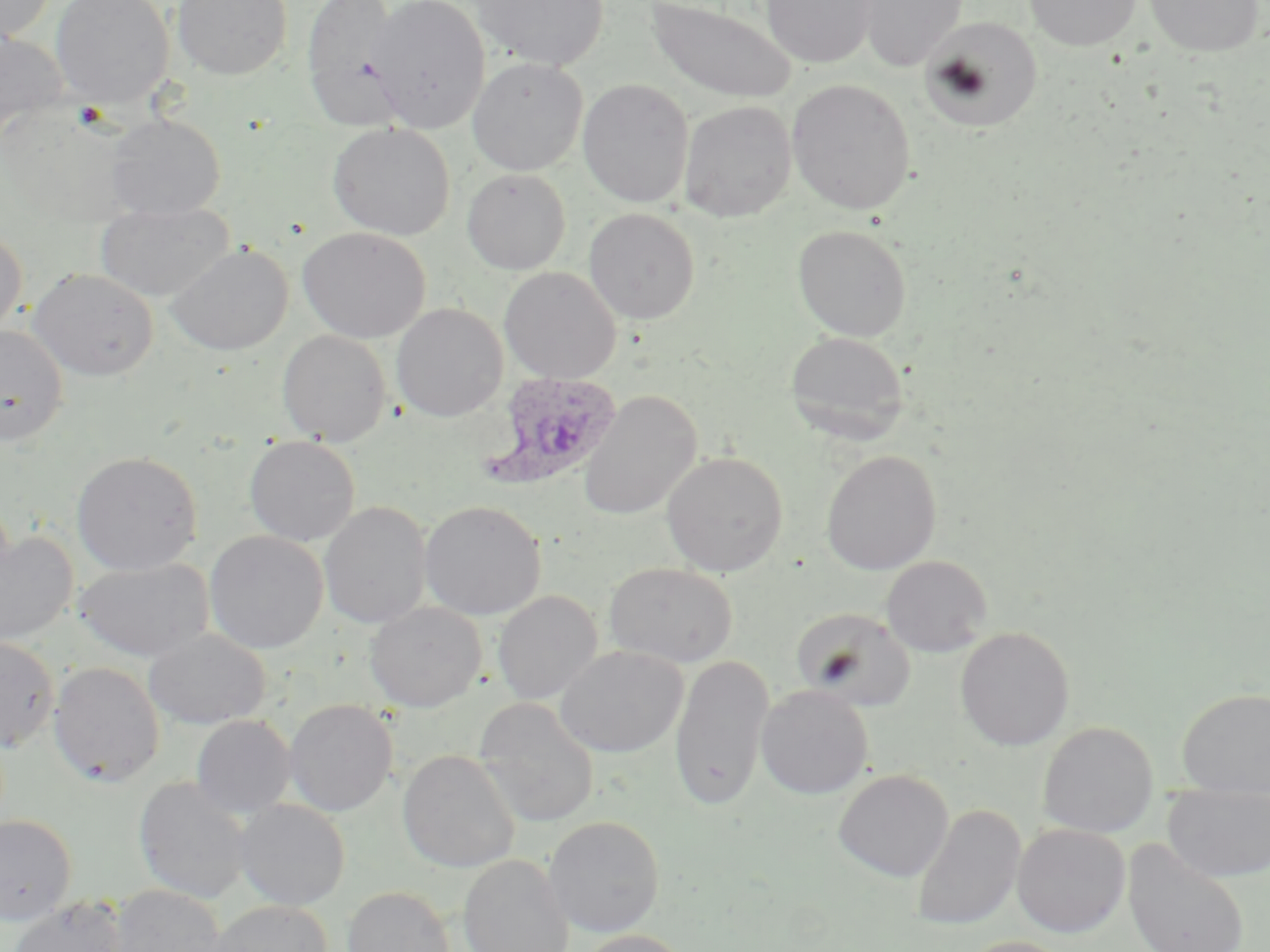

Summary:
  - Coordinate format: approximate bounding boxes as [x1, y1, x2, y2] in pixels
  - Plasmodium ovale-infected red blood cell locations: [478, 371, 623, 491]
  - Uninfected red blood cell locations: [0, 0, 55, 42], [50, 0, 175, 108], [172, 0, 292, 80], [300, 0, 409, 131], [367, 0, 490, 133], [470, 0, 609, 71], [761, 0, 876, 68], [857, 0, 965, 72], [1023, 0, 1141, 51], [1143, 0, 1264, 57], [645, 1, 797, 104], [921, 17, 1043, 132], [0, 30, 69, 145], [467, 57, 587, 175], [577, 78, 694, 208], [787, 79, 917, 215], [679, 100, 797, 223], [106, 114, 226, 221], [327, 122, 455, 240], [462, 168, 571, 274], [95, 200, 235, 302], [583, 208, 700, 324], [792, 224, 911, 341], [0, 227, 27, 337], [297, 227, 431, 342], [166, 244, 293, 355], [499, 266, 622, 384], [28, 267, 159, 381], [391, 302, 508, 421], [0, 324, 68, 446], [277, 329, 392, 446], [785, 330, 909, 443], [578, 390, 702, 521], [244, 436, 360, 546], [821, 449, 941, 575], [662, 450, 788, 576], [71, 451, 203, 575], [419, 500, 546, 620], [319, 501, 432, 629], [0, 531, 78, 647], [204, 531, 328, 654], [880, 555, 992, 657], [74, 558, 213, 662], [604, 562, 738, 667], [493, 590, 603, 705], [365, 602, 486, 712], [792, 607, 916, 710], [955, 626, 1075, 751], [143, 628, 271, 730], [0, 635, 59, 752], [555, 645, 688, 757], [669, 654, 774, 810], [48, 661, 165, 786], [755, 685, 873, 799], [1177, 688, 1270, 798], [474, 698, 599, 827], [284, 699, 397, 816], [191, 715, 295, 818], [1037, 721, 1158, 838], [397, 749, 520, 873], [833, 769, 953, 882], [133, 777, 252, 904], [1162, 782, 1270, 883], [234, 799, 350, 910], [911, 805, 1026, 931], [0, 814, 77, 924], [543, 815, 665, 937], [1012, 823, 1130, 938], [1121, 837, 1251, 952], [458, 854, 574, 952], [107, 884, 226, 952], [342, 885, 455, 952], [8, 897, 127, 952], [207, 900, 333, 952], [575, 929, 695, 952], [959, 936, 1076, 952]
  - Slide-level diagnosis: Plasmodium ovale
  - Stain: May-Grünwald-Giemsa
  - Preparation: thin blood smear
  - Magnification: 1000x
  - Modality: optical microscopy
  - Field of view: one of a larger specimen
  - Image size: 1270×952 pixels